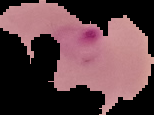 Cell region segmented out of the field of view; the surrounding area is masked to black. From a thin blood film. Image is 154×115 pixels. Malaria status: parasitized.